Identify the parasite.
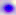
This is Toxoplasma gondii.

Photomicrograph. 400x magnification.